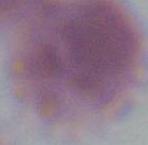 Micrograph. Captured at 1000x magnification. An erythrocyte is seen.